Classify this cell by malaria status.
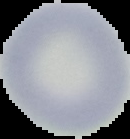

It is uninfected.

{
  "preparation": "thin blood smear",
  "image_size": "130×139 pixels",
  "image_type": "segmented cell region with the area outside set to black"
}